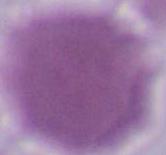

Captured at 1000x magnification. Photomicrograph. An erythrocyte is shown.